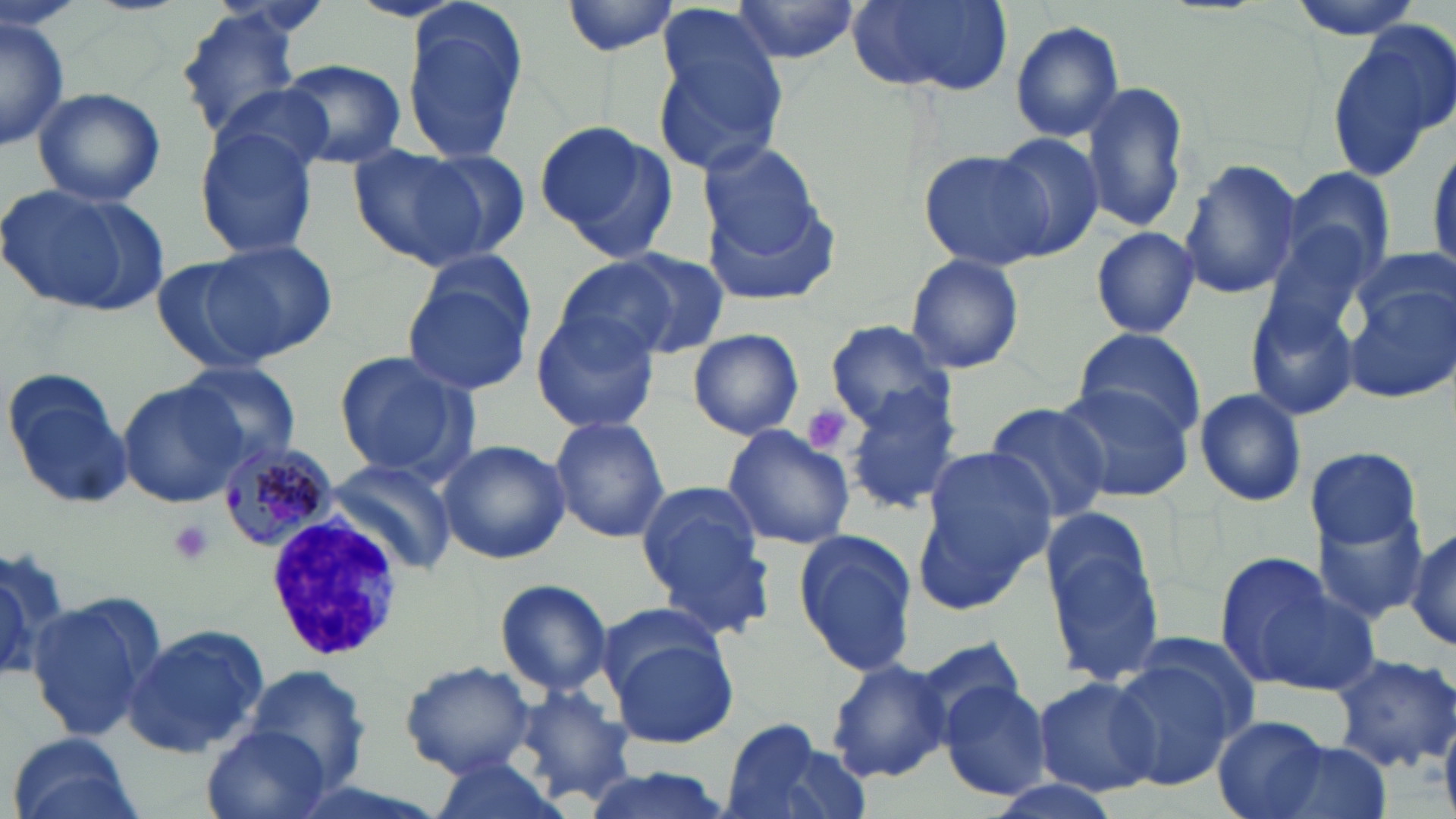

Approximate bounding boxes as (x1, y1, x2, y2) in pixels. White blood cell locations: (262, 511, 407, 663). Plasmodium malariae-infected red blood cell locations: (218, 440, 336, 556). Uninfected red blood cell locations: (561, 0, 683, 56), (728, 0, 863, 66), (849, 0, 1013, 96), (1286, 0, 1427, 39), (173, 2, 314, 145), (400, 5, 529, 168), (658, 5, 784, 110), (0, 15, 71, 154), (1326, 19, 1456, 182), (1011, 20, 1127, 141), (653, 37, 791, 174), (280, 60, 406, 168), (1081, 80, 1189, 234), (31, 86, 167, 207), (537, 122, 676, 257), (194, 127, 320, 262), (989, 133, 1104, 258), (698, 140, 831, 265), (348, 144, 495, 271), (922, 148, 1058, 272), (407, 149, 531, 263), (1178, 159, 1301, 299), (1282, 166, 1396, 289), (0, 183, 165, 317), (699, 183, 843, 310), (1090, 226, 1201, 340), (1262, 226, 1372, 345), (208, 239, 337, 358), (609, 251, 730, 357), (905, 253, 1025, 375), (149, 257, 279, 375), (554, 261, 677, 362), (402, 271, 536, 395), (1344, 273, 1456, 406), (1245, 295, 1360, 421), (531, 312, 659, 434), (826, 320, 954, 432), (687, 328, 804, 440), (1070, 328, 1206, 437), (331, 351, 477, 483), (176, 362, 299, 465), (4, 370, 133, 508), (1053, 381, 1196, 502), (119, 382, 243, 506), (845, 390, 962, 514), (1193, 390, 1307, 506), (983, 402, 1111, 525), (549, 415, 669, 543), (721, 425, 855, 550), (438, 440, 569, 564), (1303, 444, 1422, 561), (915, 445, 1055, 612), (326, 462, 453, 571), (636, 479, 770, 634), (1311, 502, 1431, 629), (1041, 511, 1168, 687), (1357, 517, 1453, 636), (1408, 527, 1456, 655), (794, 528, 918, 675), (0, 553, 59, 686), (1212, 554, 1355, 694), (494, 578, 615, 696), (26, 591, 167, 744), (594, 601, 732, 700), (121, 625, 269, 759), (1125, 628, 1266, 740), (610, 637, 738, 748), (916, 640, 1029, 735), (1328, 652, 1456, 776), (1109, 657, 1241, 791), (826, 659, 953, 783), (402, 661, 535, 776), (247, 664, 371, 793), (1032, 676, 1161, 797), (938, 680, 1053, 800), (511, 683, 635, 807), (1211, 715, 1331, 819), (719, 718, 864, 819), (198, 723, 331, 819), (6, 734, 140, 819), (1262, 741, 1392, 819), (425, 756, 565, 818), (573, 768, 742, 819), (980, 775, 1127, 819). Platelet locations: (802, 404, 852, 455), (168, 519, 216, 565). Slide-level diagnosis: Plasmodium malariae. May-Grünwald-Giemsa stain. Thin blood smear. Optical microscopy. Single field of view. Image is 1456×819 pixels. Captured at 1000x magnification.